Assess the morphology of the erythrocytes.
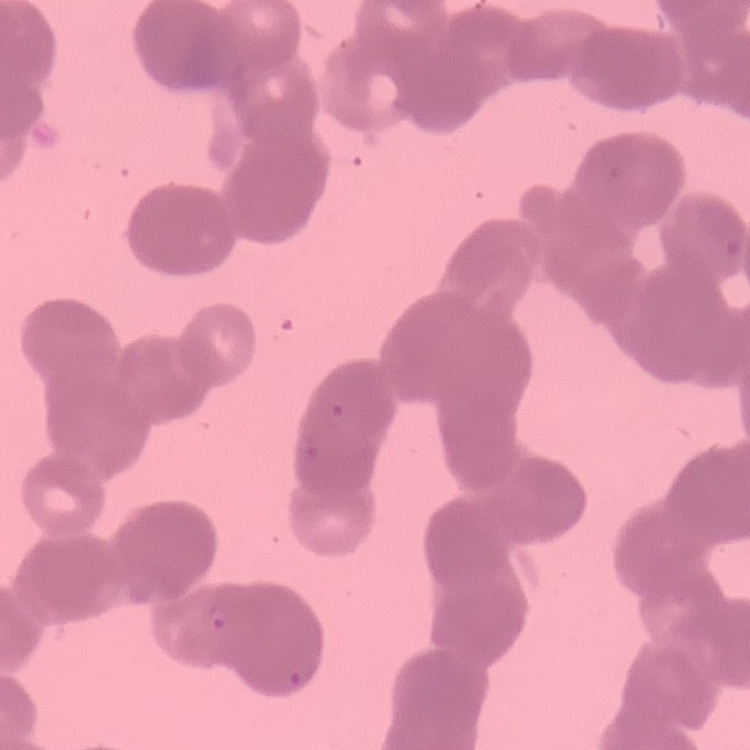

They show rouleaux formation.

preparation = thin blood smear
stain = Field's or Giemsa
image type = square crop of a larger photomicrograph